Point out each leukocyte.
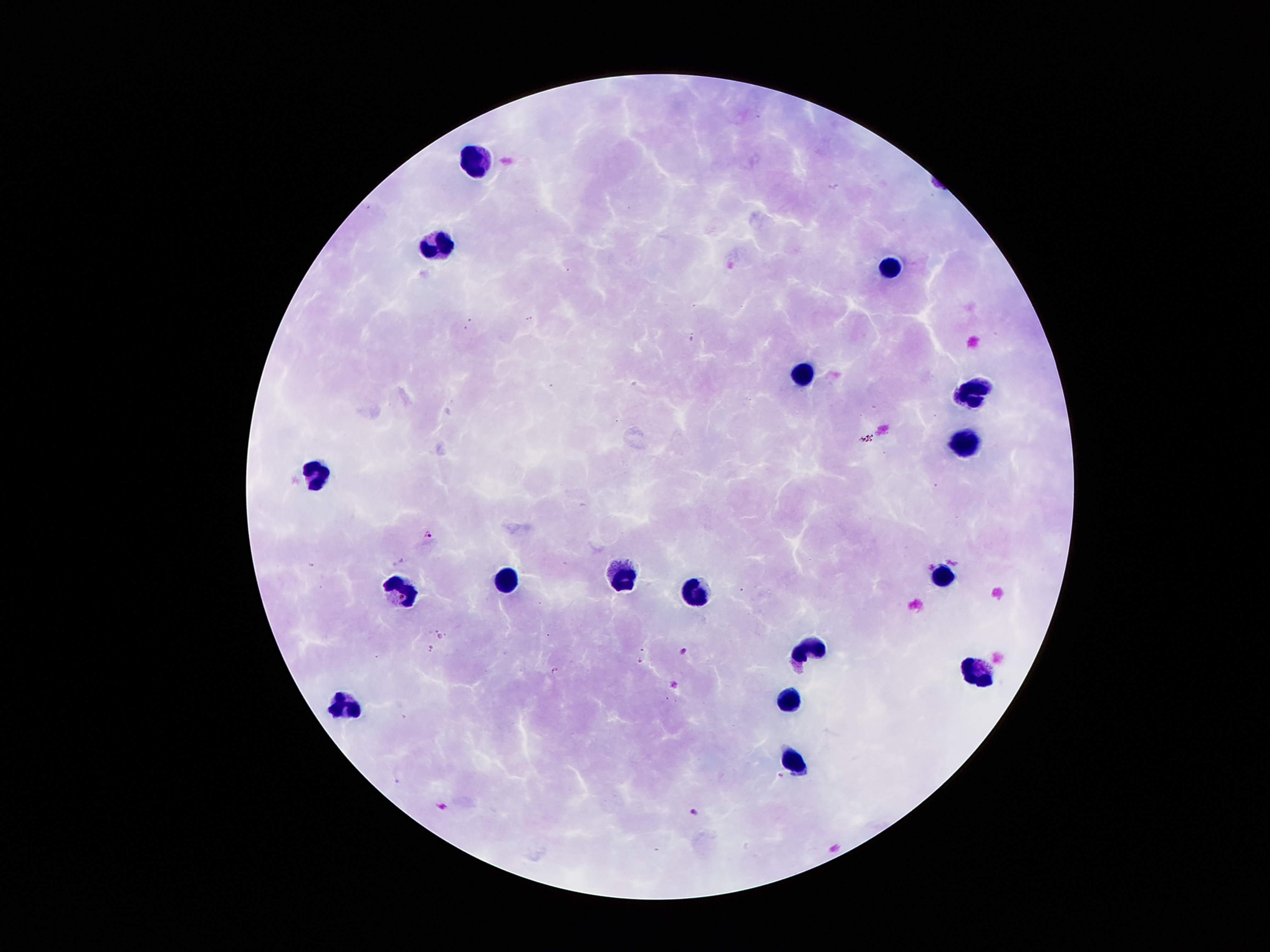
Approximate centers as [x, y] in pixels.
Leukocytes: [476, 155], [433, 243], [886, 270], [800, 375], [971, 394], [960, 443], [314, 472], [624, 577], [946, 579], [513, 586], [696, 589], [407, 592], [814, 650], [973, 668], [789, 694], [345, 705], [793, 758].

Malaria parasite locations: [833, 184], [365, 204], [528, 316], [469, 320], [465, 328], [692, 337], [552, 384], [867, 439], [935, 485], [426, 533], [440, 635], [430, 647], [641, 649], [683, 650], [638, 660], [554, 668], [781, 774], [692, 809]. Single field of view. Thick blood smear. Smartphone photograph taken through the microscope eyepiece. Image is 1270×952 pixels. 100x magnification. Giemsa stain. Patient malaria status: positive for Plasmodium falciparum.